Locate every Plasmodium falciparum-infected red blood cell.
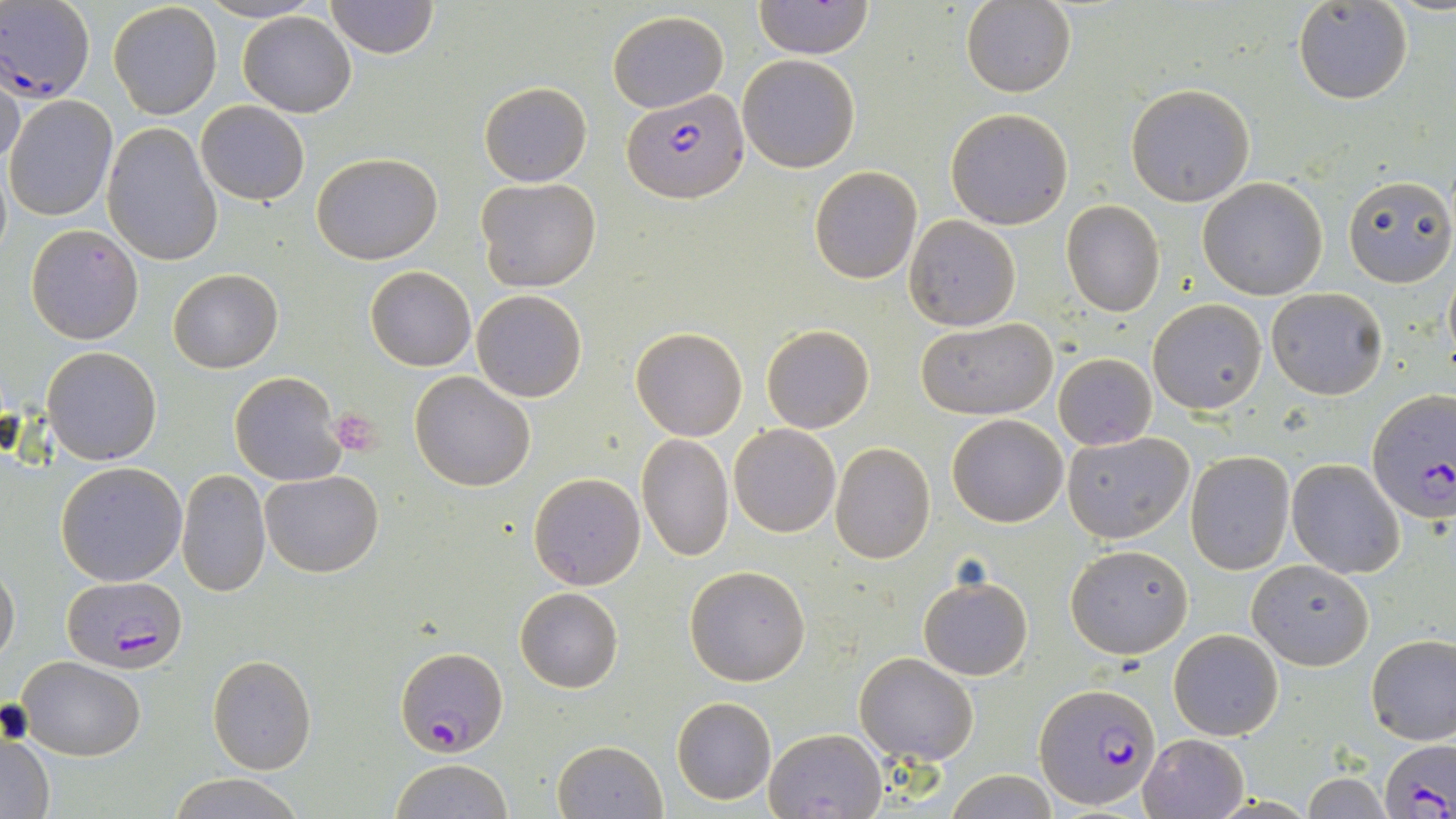
Approximate bounding boxes as named x1/y1/x2/y2 corners in pixels.
Plasmodium falciparum-infected red blood cells: (x1=0, y1=0, x2=98, y2=101), (x1=622, y1=90, x2=748, y2=204), (x1=1367, y1=389, x2=1455, y2=524), (x1=68, y1=576, x2=184, y2=671), (x1=396, y1=646, x2=505, y2=757), (x1=1034, y1=683, x2=1161, y2=809), (x1=1378, y1=737, x2=1456, y2=819).

Platelet locations: (x1=331, y1=408, x2=386, y2=458), (x1=0, y1=699, x2=33, y2=745). Uninfected red blood cell locations: (x1=324, y1=0, x2=439, y2=57), (x1=753, y1=0, x2=873, y2=61), (x1=108, y1=1, x2=223, y2=120), (x1=961, y1=1, x2=1075, y2=98), (x1=1293, y1=2, x2=1412, y2=105), (x1=238, y1=11, x2=356, y2=117), (x1=607, y1=11, x2=729, y2=111), (x1=737, y1=55, x2=860, y2=172), (x1=1, y1=69, x2=26, y2=172), (x1=479, y1=81, x2=593, y2=186), (x1=1124, y1=83, x2=1255, y2=206), (x1=6, y1=95, x2=118, y2=222), (x1=196, y1=101, x2=310, y2=204), (x1=946, y1=107, x2=1074, y2=229), (x1=102, y1=123, x2=222, y2=266), (x1=311, y1=152, x2=443, y2=264), (x1=809, y1=165, x2=922, y2=285), (x1=1342, y1=174, x2=1455, y2=288), (x1=476, y1=177, x2=601, y2=292), (x1=1197, y1=177, x2=1330, y2=301), (x1=1062, y1=201, x2=1165, y2=317), (x1=903, y1=215, x2=1021, y2=331), (x1=26, y1=223, x2=143, y2=343), (x1=366, y1=266, x2=476, y2=371), (x1=168, y1=269, x2=283, y2=373), (x1=1266, y1=287, x2=1389, y2=400), (x1=472, y1=289, x2=588, y2=403), (x1=1148, y1=298, x2=1267, y2=415), (x1=915, y1=317, x2=1058, y2=420), (x1=761, y1=324, x2=874, y2=433), (x1=629, y1=327, x2=747, y2=442), (x1=43, y1=346, x2=162, y2=465), (x1=1053, y1=352, x2=1156, y2=449), (x1=229, y1=371, x2=346, y2=487), (x1=410, y1=371, x2=536, y2=492), (x1=946, y1=413, x2=1069, y2=528), (x1=729, y1=424, x2=841, y2=538), (x1=1063, y1=430, x2=1195, y2=544), (x1=637, y1=433, x2=734, y2=562), (x1=829, y1=443, x2=935, y2=564), (x1=1185, y1=450, x2=1295, y2=574), (x1=1287, y1=457, x2=1404, y2=578), (x1=56, y1=461, x2=187, y2=586), (x1=260, y1=468, x2=384, y2=577), (x1=177, y1=469, x2=271, y2=597), (x1=528, y1=472, x2=646, y2=591), (x1=1066, y1=543, x2=1192, y2=659), (x1=1248, y1=559, x2=1374, y2=671), (x1=0, y1=560, x2=19, y2=664), (x1=684, y1=565, x2=811, y2=686), (x1=918, y1=575, x2=1033, y2=679), (x1=514, y1=586, x2=623, y2=693), (x1=1168, y1=629, x2=1285, y2=741), (x1=1366, y1=634, x2=1456, y2=744), (x1=855, y1=652, x2=979, y2=765), (x1=16, y1=655, x2=147, y2=760), (x1=207, y1=655, x2=317, y2=774), (x1=672, y1=696, x2=776, y2=805), (x1=766, y1=727, x2=887, y2=819), (x1=0, y1=734, x2=56, y2=818), (x1=1140, y1=734, x2=1248, y2=818), (x1=553, y1=740, x2=667, y2=818), (x1=388, y1=758, x2=511, y2=819), (x1=942, y1=770, x2=1062, y2=818), (x1=166, y1=772, x2=306, y2=819), (x1=1299, y1=774, x2=1393, y2=816). Slide-level diagnosis: Plasmodium falciparum. Single field of view. Light microscopy. Thin blood film. Captured at 1000x magnification. May-Grünwald-Giemsa stain. Image is 1456×819 pixels.